Locate every malaria parasite and every leukocyte.
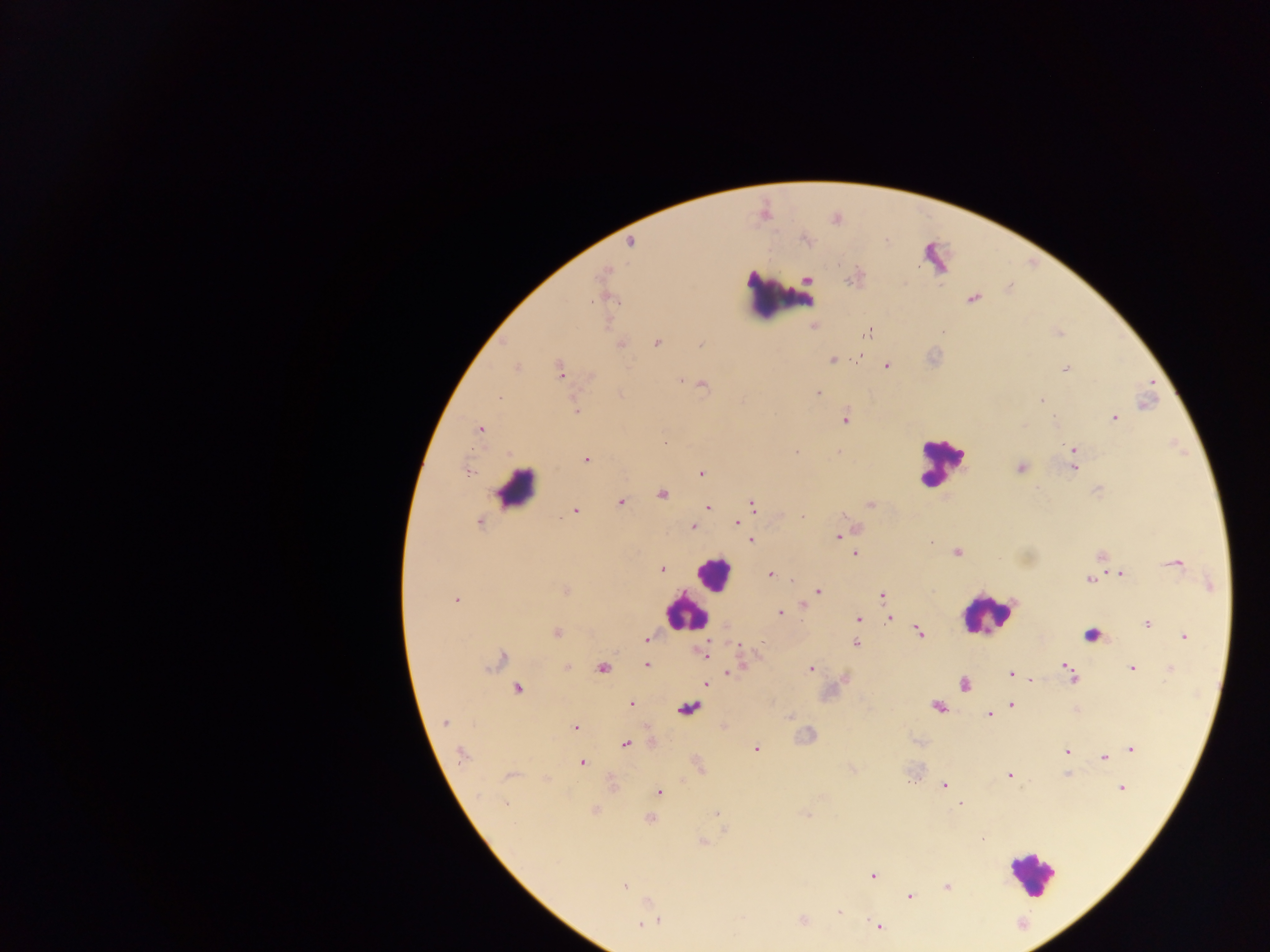

Approximate centers as x y in pixels.
Malaria parasites: 805 241; 629 244; 592 300; 942 332; 1059 332; 867 334; 656 342; 703 343; 619 344; 858 357; 832 360; 886 366; 517 367; 1067 369; 560 370; 678 378; 703 385; 819 391; 622 393; 500 395; 1040 401; 576 409; 846 417; 1055 419; 1115 419; 481 430; 663 440; 1075 448; 796 451; 839 452; 585 458; 1020 467; 1075 467; 468 471; 703 471; 1098 490; 662 495; 622 503; 869 503; 752 504; 708 505; 576 513; 803 516; 480 521; 735 521; 693 527; 836 535; 750 540; 931 540; 853 551; 956 552; 1101 555; 1178 564; 661 569; 1121 573; 770 574; 775 574; 1089 579; 818 591; 880 595; 454 596; 803 605; 781 614; 891 618; 860 619; 1148 624; 918 631; 557 633; 1184 635; 646 639; 854 643; 707 656; 502 660; 647 662; 1063 664; 565 666; 602 669; 1132 669; 812 670; 729 671; 1009 672; 1072 678; 1031 679; 963 684; 706 685; 517 689; 1011 703; 631 704; 937 706; 989 715; 788 717; 446 722; 576 726; 626 742; 756 750; 1067 751; 1133 751; 461 756; 1103 756; 582 762; 852 769; 1008 772; 1067 775; 913 778; 944 786; 1121 786; 658 794; 505 804; 961 806; 716 813; 805 814; 649 818; 725 830; 981 837; 703 842; 871 877; 946 885; 624 886; 910 897; 647 901; 839 912; 802 919; 658 921; 640 924; 879 927.
Leukocytes: 789 293; 937 464; 521 490; 714 575; 993 613; 682 615; 1033 883.

Thick blood smear. Image is 1270×952 pixels. Mobile-phone photograph taken through the microscope. Collected in Ghana. Single field of view.